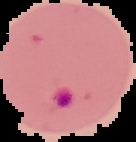

Summary:
  - Preparation: thin blood smear
  - Image type: segmented cell region with the area outside set to black
  - Image size: 136×142 pixels
  - Malaria status: parasitized